Report the malaria status of this cell.
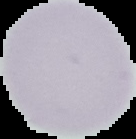

Uninfected.

preparation = thin blood film
image size = 136×139 pixels
image type = segmented cell region on a black background